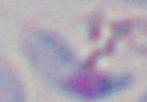

Toxoplasma gondii is seen. Captured at 1000x magnification. Photomicrograph.